Report the malaria status of this cell.
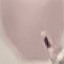

It is uninfected.

image type = automatically extracted cell patch, resized to 64 × 64 pixels
stain = Giemsa
capture = smartphone camera at the microscope eyepiece
preparation = thin smear